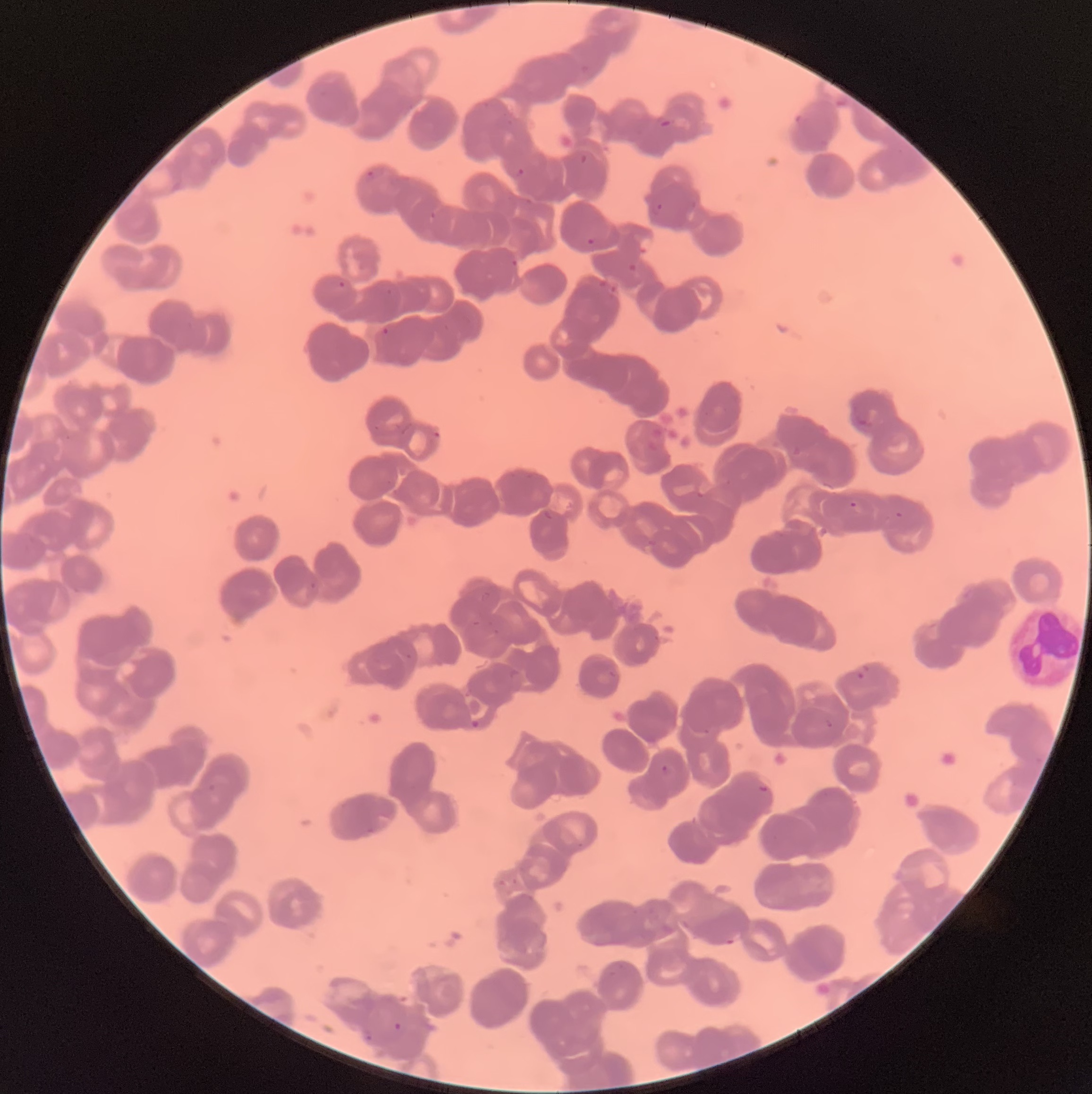
coordinate format = approximate bounding boxes as [x1, y1, x2, y2] in pixels
Plasmodium parasite locations = [659, 119, 673, 130], [579, 154, 588, 164], [515, 167, 525, 178], [365, 169, 376, 183], [649, 202, 664, 215], [429, 209, 437, 220], [637, 234, 655, 257], [586, 237, 595, 246], [511, 259, 519, 267], [626, 263, 639, 274], [597, 277, 607, 289], [337, 281, 346, 289], [385, 287, 393, 295], [382, 326, 390, 336], [855, 418, 871, 432], [697, 483, 712, 500], [848, 500, 859, 509], [894, 510, 905, 520], [855, 671, 866, 681], [468, 718, 483, 731], [824, 719, 835, 729], [657, 763, 673, 776], [757, 782, 769, 794], [724, 935, 738, 946], [392, 1019, 403, 1032], [363, 1032, 375, 1042]
modality = optical microscopy
image size = 1092×1094 pixels
red blood cell morphology = rouleaux formation
preparation = thin blood smear